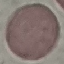

malaria status = uninfected
capture = smartphone through the microscope eyepiece
stain = Giemsa
image type = cell patch, automatically extracted from a larger field of view and resized to 64 × 64 pixels
preparation = thin blood smear